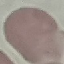 Malaria status: uninfected. Thin blood smear. Automatically extracted cell patch, resized to 64 × 64 pixels. Acquired by smartphone through the microscope eyepiece. Giemsa stain.